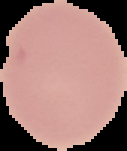

Segmented cell region on a black background. From a thin blood smear. Image is 127×151 pixels. Malaria status: uninfected.